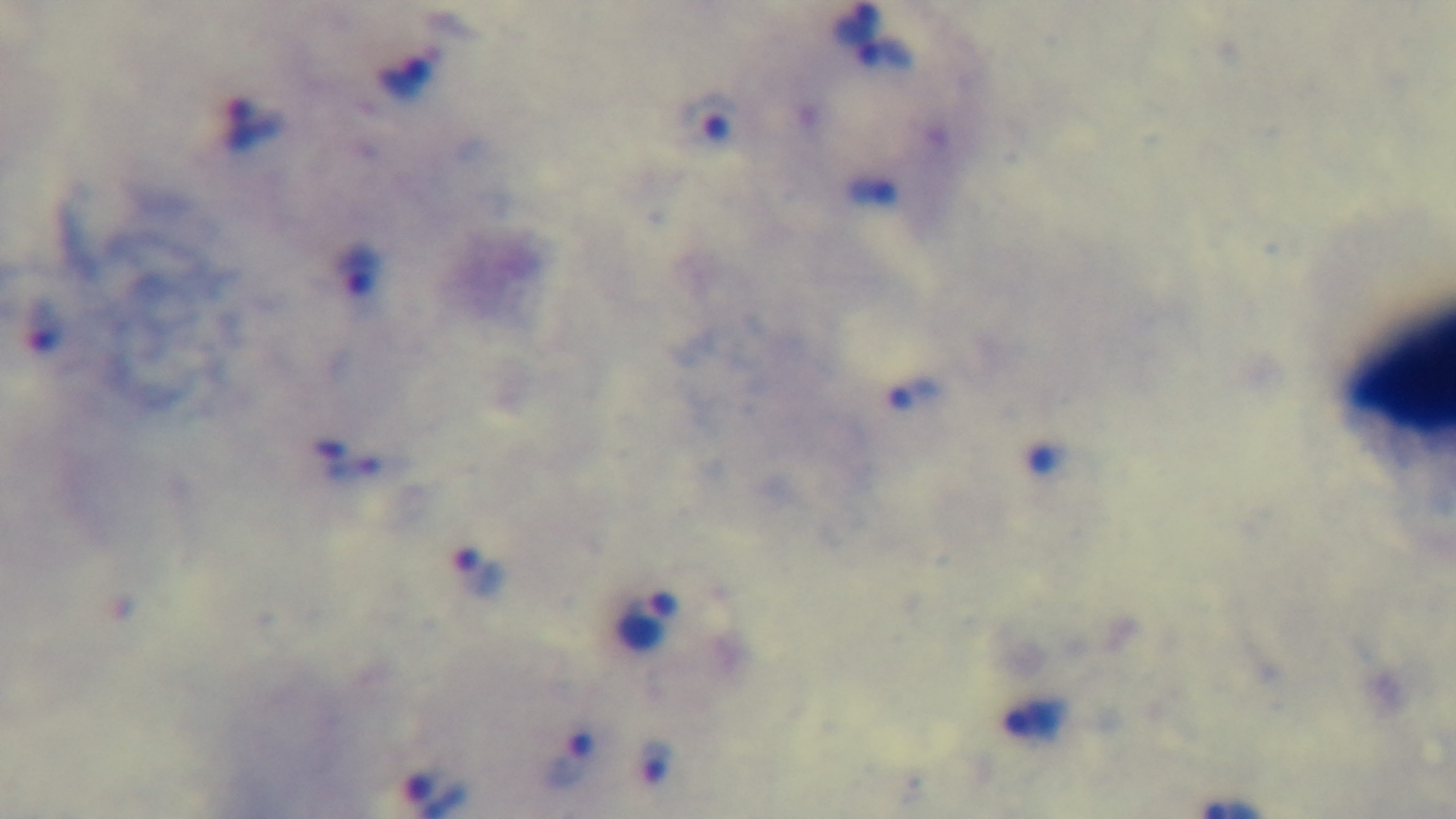

{
  "modality": "light microscopy",
  "capture": "mounted 4K digital camera",
  "field_of_view": "one from the slide",
  "objective": "100x oil immersion",
  "malaria_status": "infected",
  "stain": "Giemsa",
  "preparation": "thick blood film"
}